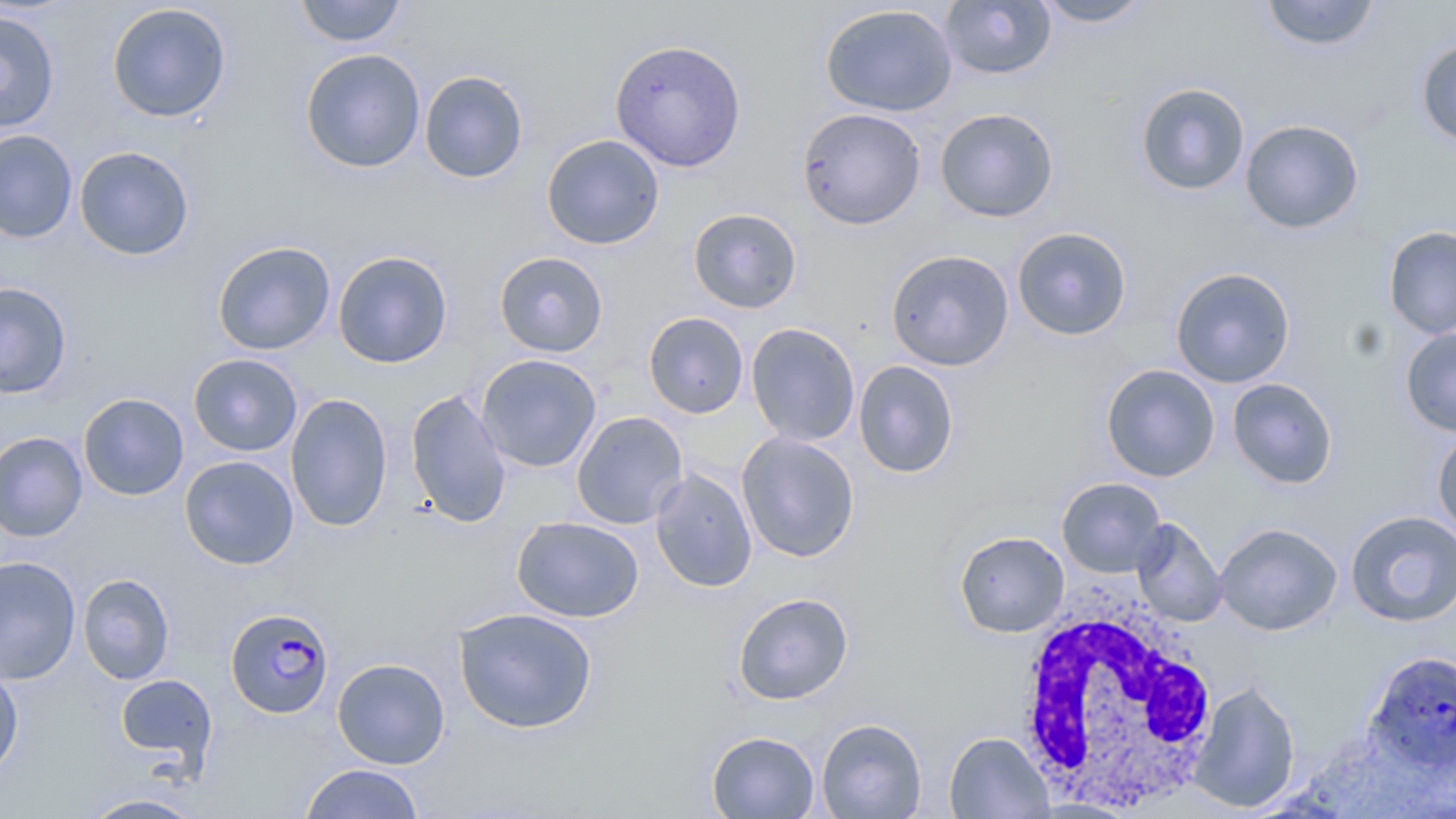

slide-level diagnosis = Plasmodium falciparum
field of view = one of a larger specimen
Plasmodium falciparum-infected red blood cell locations = approximate bounding boxes as (x1, y1, x2, y2) in pixels: (225, 607, 334, 719), (1363, 650, 1456, 774)
stain = May-Grünwald-Giemsa
image size = 1456×819 pixels
preparation = thin blood smear
uninfected red blood cell locations = approximate bounding boxes as (x1, y1, x2, y2) in pixels: (293, 0, 408, 47), (1032, 0, 1154, 28), (1259, 0, 1382, 52), (939, 1, 1056, 81), (106, 3, 232, 123), (819, 3, 958, 117), (0, 10, 60, 134), (1415, 38, 1456, 148), (609, 39, 747, 172), (300, 48, 426, 173), (419, 70, 529, 184), (1135, 82, 1250, 196), (796, 107, 926, 230), (935, 107, 1060, 223), (1240, 119, 1365, 234), (0, 129, 78, 243), (540, 134, 665, 249), (75, 146, 195, 261), (688, 207, 803, 313), (1383, 225, 1456, 339), (1012, 227, 1132, 341), (212, 241, 336, 355), (885, 249, 1015, 371), (332, 250, 454, 369), (494, 251, 609, 358), (1170, 267, 1296, 388), (0, 282, 72, 399), (643, 312, 749, 418), (746, 322, 861, 446), (1400, 327, 1456, 436), (188, 353, 303, 456), (476, 354, 602, 472), (853, 360, 959, 479), (1101, 363, 1221, 482), (1227, 377, 1339, 489), (405, 389, 512, 528), (285, 392, 393, 532), (78, 393, 189, 501), (571, 410, 688, 529), (1432, 429, 1456, 542), (0, 432, 88, 542), (736, 432, 860, 563), (179, 455, 299, 570), (649, 468, 757, 593), (1056, 477, 1167, 578), (1345, 510, 1456, 628), (512, 516, 644, 623), (1131, 518, 1228, 627), (1215, 522, 1343, 636), (955, 531, 1069, 637), (0, 555, 81, 685), (77, 573, 175, 685), (732, 592, 854, 705), (453, 607, 599, 734), (332, 658, 450, 769), (0, 662, 24, 781), (115, 673, 217, 772), (1189, 679, 1301, 813), (816, 718, 927, 818), (706, 730, 820, 818), (944, 732, 1054, 818), (299, 763, 425, 818), (77, 792, 210, 818)
magnification = 1000x
modality = optical microscopy
white blood cell locations = approximate bounding boxes as (x1, y1, x2, y2) in pixels: (1011, 590, 1221, 811)